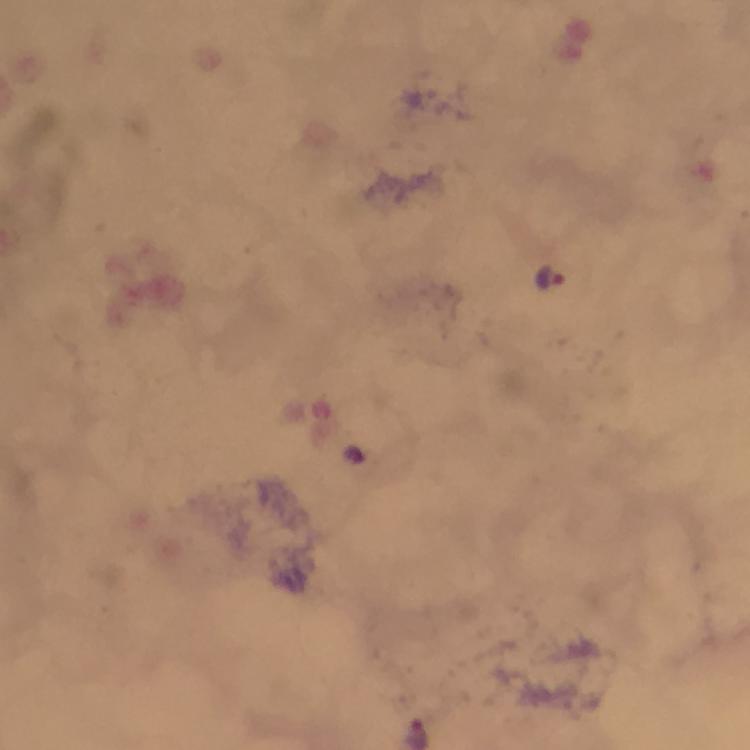
{
  "cropped_from": "a single field of view",
  "magnification": "100x",
  "stain": "Giemsa",
  "preparation": "thick smear",
  "immersion_oil": "applied",
  "image_size": "750×750 pixels",
  "capture": "smartphone photograph through a microscope",
  "plasmodium_parasite_locations": "approximate centers as (x, y) in pixels: (549, 279)",
  "context": "from a malaria diagnostic workup"
}